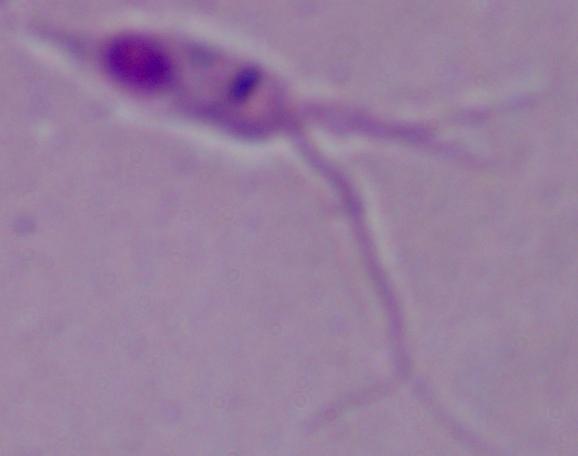 Micrograph. Captured at 1000x magnification. A Leishmania parasite is seen.